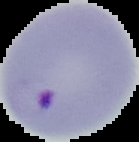
Summary:
  - Image size: 139×142 pixels
  - Preparation: thin blood film
  - Malaria status: parasitized
  - Image type: segmented cell region with the area outside set to black